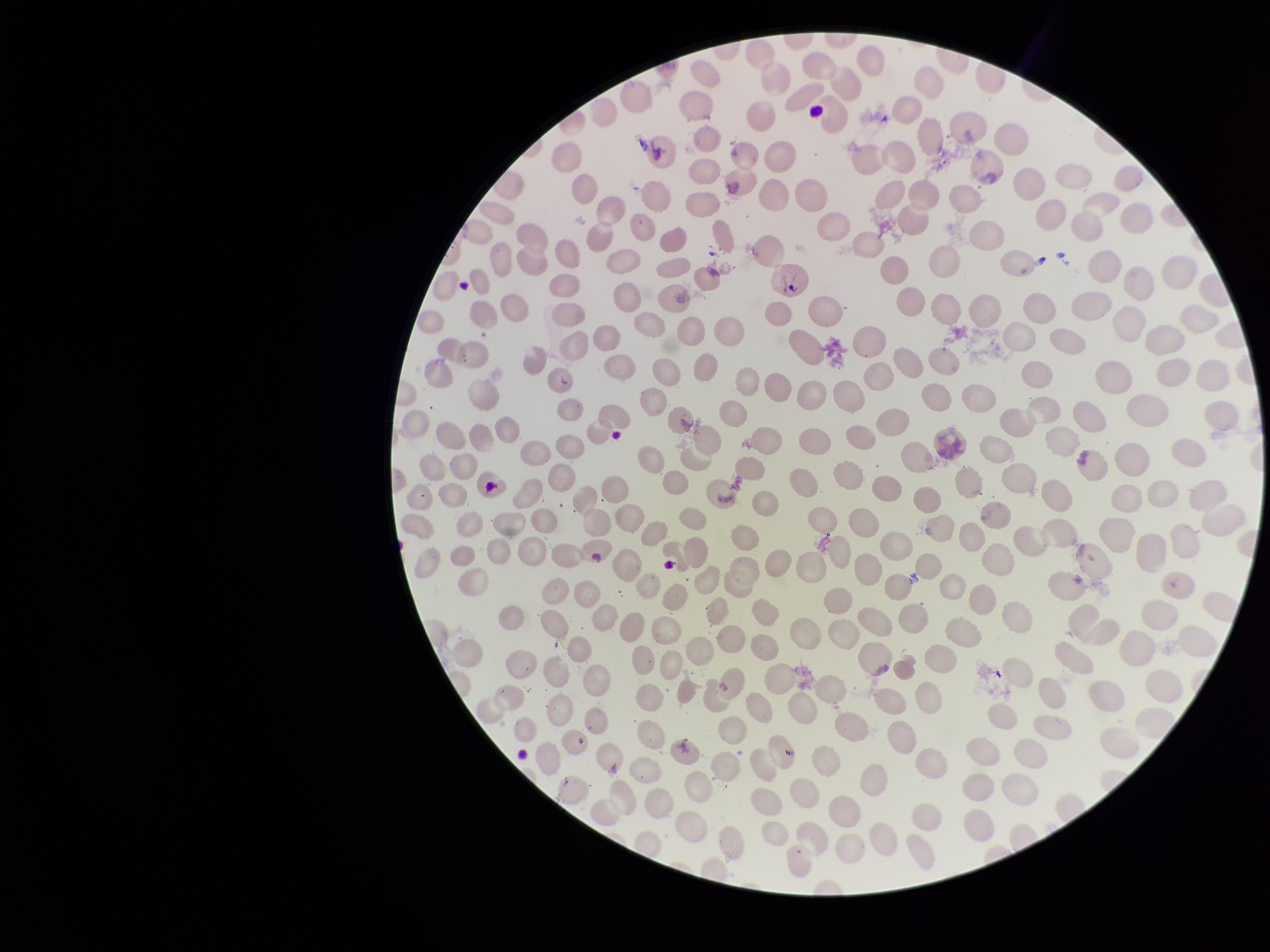
Summary:
  - Parasitized red blood cells: none detected
  - Patient malaria status: infected
  - Field of view: one from this slide
  - Image size: 1270×952 pixels
  - Capture: smartphone photograph through the microscope eyepiece
  - Red blood cell count: 258
  - Stain: Giemsa
  - Preparation: thin blood smear
  - Species reported for this patient: Plasmodium vivax
  - Parasitized red blood cell count: 0